State which cell type is depicted.
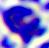
A leukocyte.

Photomicrograph. Captured at 400x magnification.